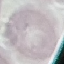
result = no malaria parasites detected
image type = automatically extracted cell patch, resized to 64 × 64 pixels
capture = smartphone camera at the microscope eyepiece
stain = Giemsa
preparation = thin blood film